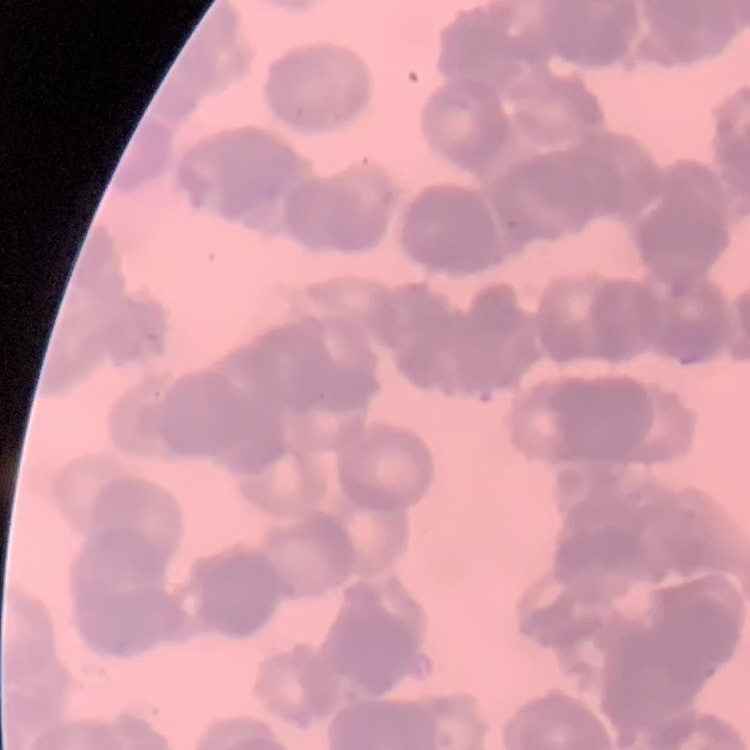 The red blood cells show rouleaux formation. Stained with either Field's or Giemsa. Square crop of a larger photomicrograph. Thin peripheral smear.